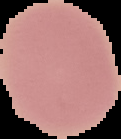

Summary:
  - Image size: 121×139 pixels
  - Malaria status: uninfected
  - Image type: segmented cell region with the area outside set to black
  - Preparation: thin blood smear